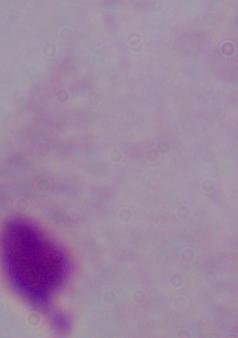 A trichomonad is shown. Captured at 1000x magnification. Micrograph.